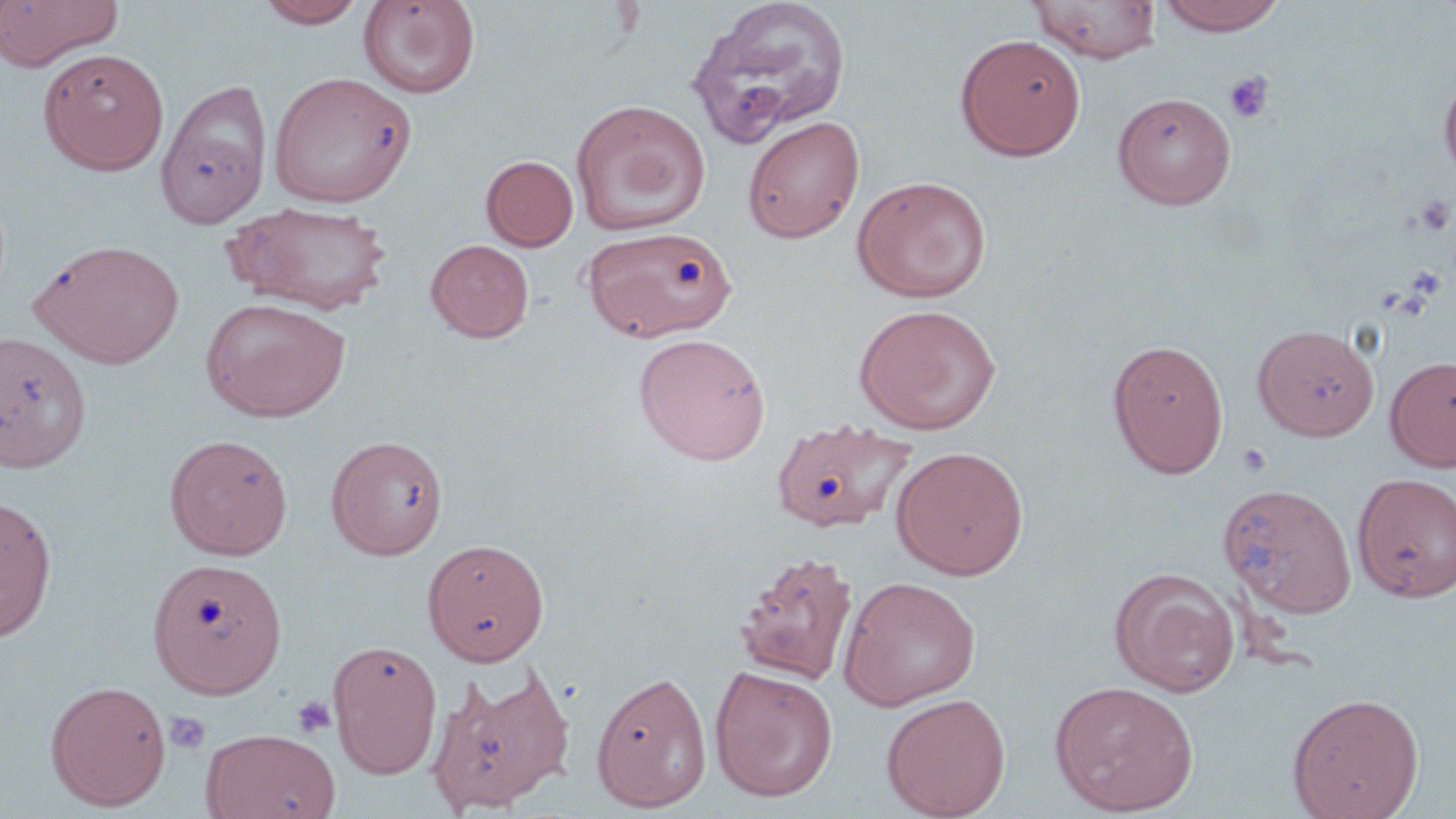

{
  "slide_level_diagnosis": "no evidence of blood parasites",
  "platelet_locations": "approximate bounding boxes as named x1/y1/x2/y2 corners in pixels: (x1=1224, y1=71, x2=1274, y2=123), (x1=292, y1=696, x2=335, y2=738), (x1=165, y1=711, x2=209, y2=755)",
  "uninfected_red_blood_cell_locations": "approximate bounding boxes as named x1/y1/x2/y2 corners in pixels: (x1=255, y1=0, x2=367, y2=28), (x1=688, y1=0, x2=851, y2=147), (x1=1156, y1=0, x2=1287, y2=35), (x1=0, y1=1, x2=122, y2=69), (x1=358, y1=1, x2=481, y2=99), (x1=1028, y1=1, x2=1162, y2=63), (x1=955, y1=33, x2=1086, y2=161), (x1=38, y1=48, x2=169, y2=175), (x1=1439, y1=71, x2=1456, y2=191), (x1=269, y1=72, x2=417, y2=208), (x1=156, y1=79, x2=273, y2=229), (x1=1113, y1=91, x2=1237, y2=210), (x1=570, y1=99, x2=712, y2=236), (x1=742, y1=116, x2=865, y2=243), (x1=481, y1=155, x2=579, y2=251), (x1=851, y1=175, x2=992, y2=303), (x1=225, y1=202, x2=393, y2=316), (x1=582, y1=226, x2=736, y2=343), (x1=30, y1=238, x2=185, y2=368), (x1=425, y1=239, x2=535, y2=343), (x1=200, y1=297, x2=350, y2=422), (x1=854, y1=303, x2=1001, y2=435), (x1=1252, y1=324, x2=1380, y2=440), (x1=1, y1=332, x2=92, y2=473), (x1=634, y1=333, x2=770, y2=465), (x1=1107, y1=338, x2=1230, y2=478), (x1=1385, y1=355, x2=1456, y2=471), (x1=771, y1=416, x2=916, y2=533), (x1=164, y1=433, x2=293, y2=560), (x1=326, y1=435, x2=448, y2=560), (x1=891, y1=446, x2=1029, y2=580), (x1=1352, y1=473, x2=1456, y2=602), (x1=1216, y1=482, x2=1356, y2=618), (x1=0, y1=495, x2=57, y2=643), (x1=422, y1=538, x2=549, y2=666), (x1=735, y1=551, x2=858, y2=685), (x1=147, y1=556, x2=287, y2=698), (x1=1108, y1=566, x2=1241, y2=696), (x1=838, y1=576, x2=980, y2=710), (x1=328, y1=638, x2=443, y2=779), (x1=426, y1=664, x2=575, y2=812), (x1=709, y1=665, x2=838, y2=802), (x1=591, y1=670, x2=712, y2=813), (x1=45, y1=679, x2=171, y2=810), (x1=1049, y1=680, x2=1200, y2=816), (x1=1287, y1=692, x2=1424, y2=819), (x1=881, y1=693, x2=1011, y2=818), (x1=201, y1=728, x2=339, y2=819)",
  "stain": "May-Grünwald-Giemsa",
  "field_of_view": "one of a larger specimen",
  "preparation": "thin blood smear",
  "image_size": "1456×819 pixels",
  "modality": "light microscopy",
  "magnification": "1000x"
}